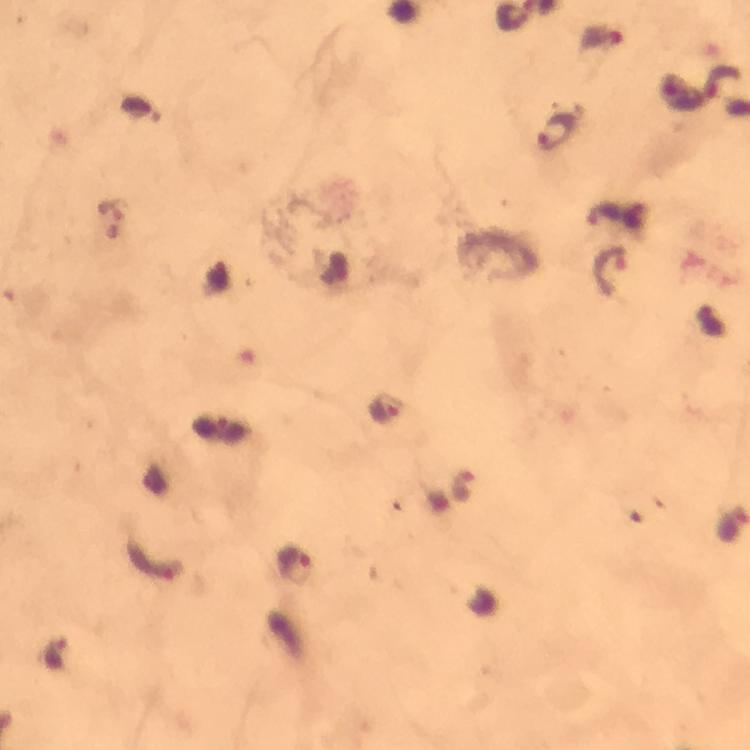

Approximate centers as [x, y] in pixels.
Summary:
  - Plasmodium parasite locations: [601, 38], [556, 130], [111, 217], [610, 268], [387, 409], [461, 487], [294, 563]
  - Stain: Giemsa
  - Magnification: 100x
  - Immersion oil: used
  - Cropped from: a single field of view
  - Image size: 750×750 pixels
  - Context: from a malaria diagnostic workup
  - Capture: smartphone mounted on the microscope
  - Preparation: thick blood smear